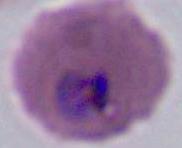
Summary:
  - Modality: micrograph
  - Identification: Plasmodium
  - Magnification: 400x or 1000x